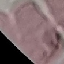
Malaria status: uninfected. Thin smear of blood. Photographed with a smartphone camera at the microscope eyepiece. Automatically extracted cell patch, resized to 64 × 64 pixels. Giemsa stain.